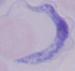
1000x magnification. Micrograph. A trypanosome is shown.